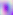
identification = Toxoplasma gondii
modality = photomicrograph
magnification = 400x